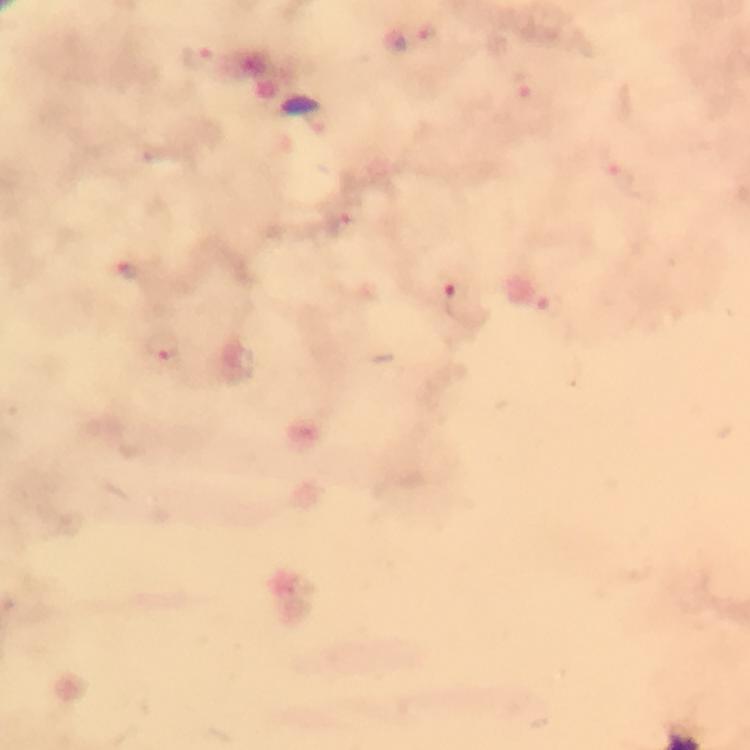

capture = smartphone camera through the microscope
preparation = thick smear
Plasmodium parasite locations = approximate centers as [x, y] in pixels: [427, 35], [199, 59], [525, 85], [622, 178], [346, 227], [129, 273], [458, 301], [164, 349]
stain = Giemsa
context = from a malaria diagnostic workup
cropped from = one field of view
magnification = 100x
immersion oil = used
image size = 750×750 pixels